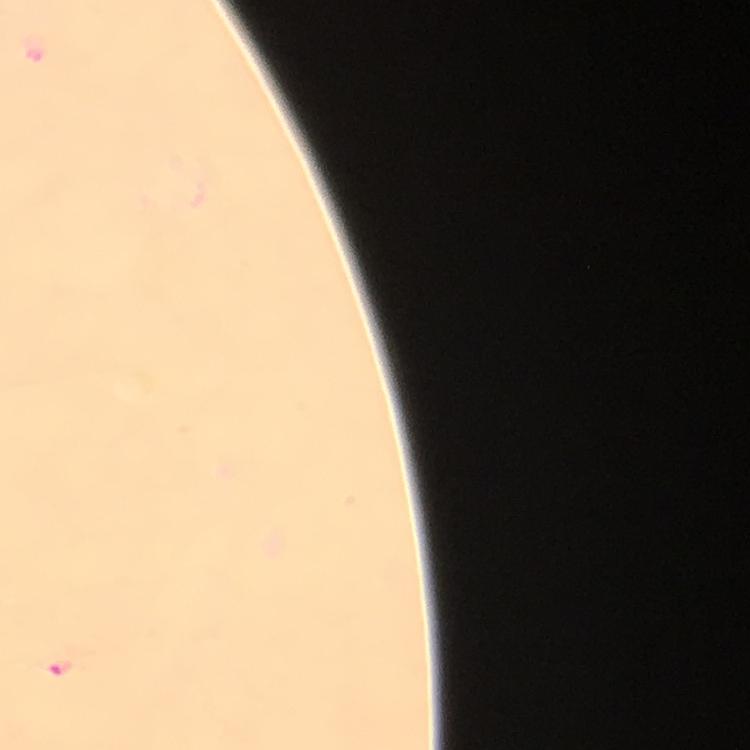
Approximate object centers, in pixels from the top-left corner. Plasmodium parasite locations: (x=58, y=666). Image is 750×750 pixels. A crop from one field of view. Giemsa-stained preparation. 100x magnification. Thick blood smear. Photographed with a smartphone mounted on the microscope. Immersion oil was used. From a malaria diagnostic workup.